Describe the morphology of the erythrocytes.
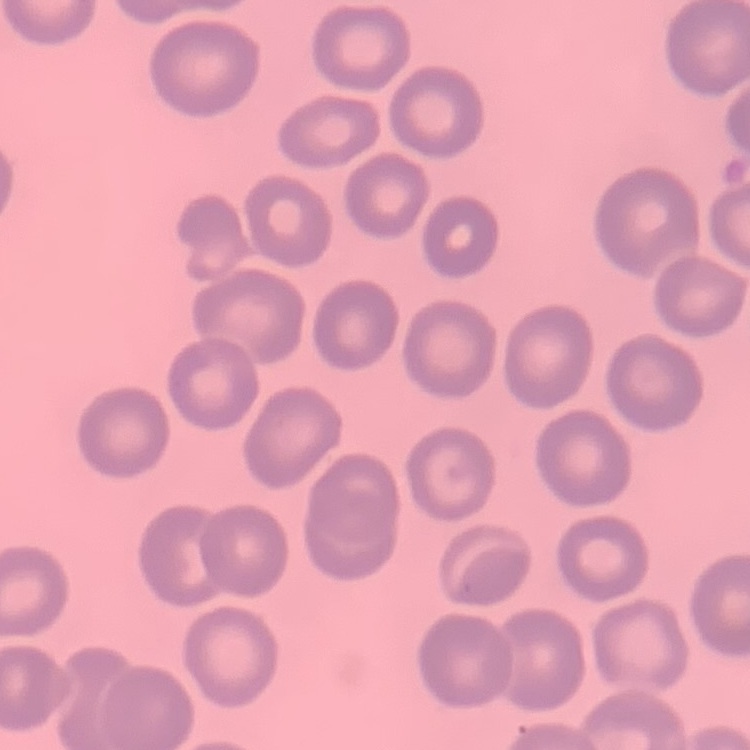
No rouleaux formation.

Thin blood smear. Stained with either Field's or Giemsa. One tile cut from a larger photomicrograph.